Identify the parasite.
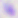
Toxoplasma gondii.

Summary:
  - Modality: micrograph
  - Magnification: 400x